Outline each uninfected red blood cell.
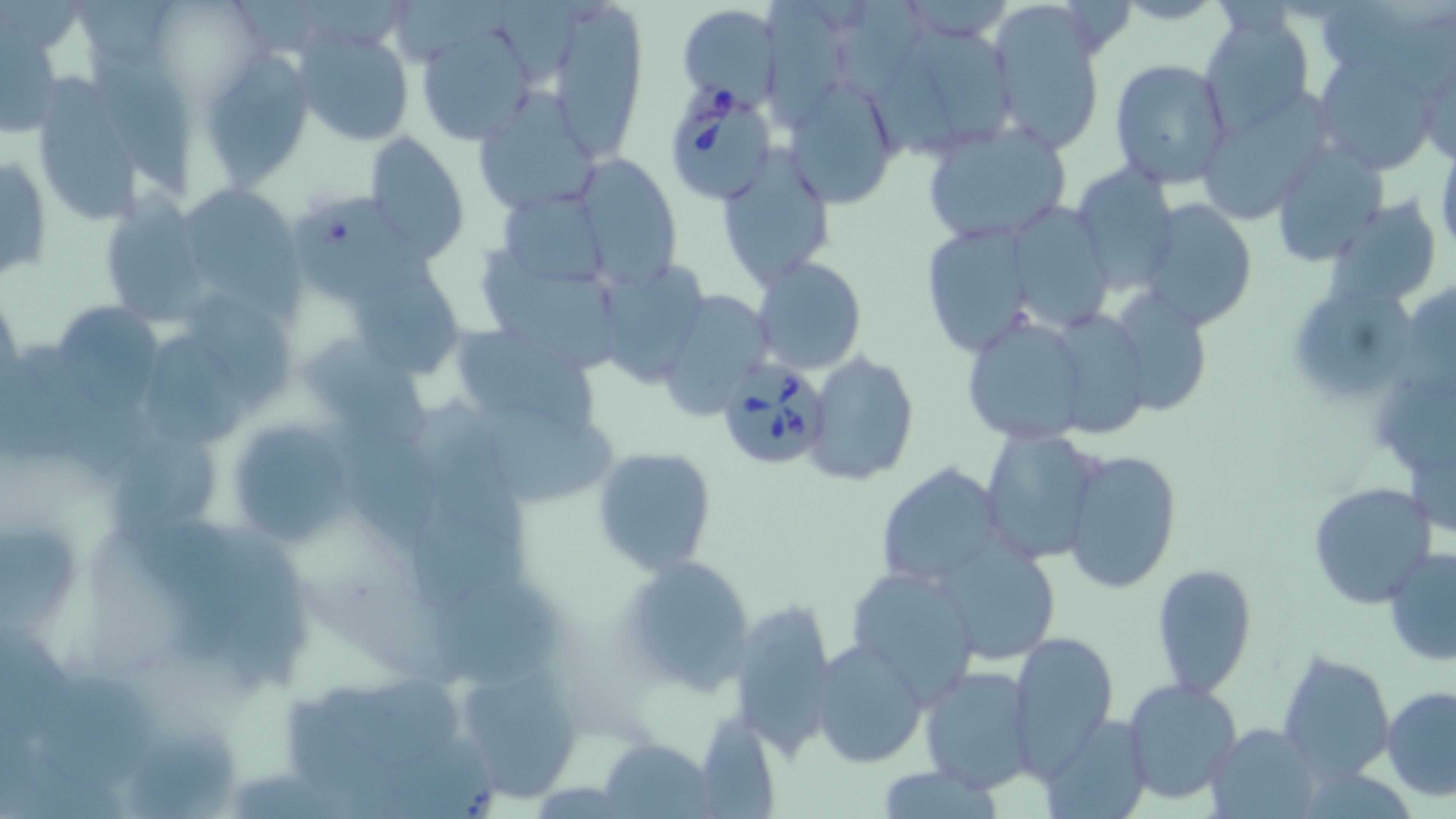
Approximate bounding boxes as named x1/y1/x2/y2 corners in pixels.
Uninfected red blood cells: (x1=548, y1=0, x2=648, y2=152), (x1=759, y1=3, x2=858, y2=128), (x1=986, y1=4, x2=1105, y2=157), (x1=677, y1=5, x2=779, y2=108), (x1=1199, y1=8, x2=1318, y2=137), (x1=914, y1=20, x2=1026, y2=145), (x1=414, y1=23, x2=536, y2=146), (x1=2, y1=24, x2=64, y2=135), (x1=295, y1=29, x2=414, y2=149), (x1=86, y1=43, x2=200, y2=201), (x1=199, y1=51, x2=315, y2=186), (x1=1313, y1=51, x2=1439, y2=173), (x1=1416, y1=52, x2=1455, y2=166), (x1=1109, y1=58, x2=1233, y2=189), (x1=785, y1=78, x2=900, y2=207), (x1=30, y1=79, x2=151, y2=230), (x1=472, y1=88, x2=603, y2=216), (x1=920, y1=122, x2=1073, y2=244), (x1=363, y1=131, x2=470, y2=263), (x1=1435, y1=141, x2=1456, y2=267), (x1=1271, y1=142, x2=1389, y2=267), (x1=716, y1=150, x2=835, y2=288), (x1=1, y1=154, x2=52, y2=282), (x1=574, y1=155, x2=681, y2=282), (x1=1069, y1=166, x2=1180, y2=295), (x1=184, y1=180, x2=310, y2=326), (x1=500, y1=191, x2=607, y2=290), (x1=98, y1=196, x2=211, y2=326), (x1=1329, y1=196, x2=1442, y2=308), (x1=1136, y1=197, x2=1258, y2=332), (x1=292, y1=198, x2=414, y2=302), (x1=1007, y1=201, x2=1118, y2=331), (x1=918, y1=221, x2=1037, y2=358), (x1=483, y1=245, x2=620, y2=366), (x1=346, y1=253, x2=459, y2=377), (x1=753, y1=256, x2=867, y2=374), (x1=603, y1=261, x2=707, y2=388), (x1=1298, y1=284, x2=1415, y2=402), (x1=1105, y1=289, x2=1213, y2=417), (x1=657, y1=291, x2=772, y2=418), (x1=58, y1=298, x2=164, y2=412), (x1=961, y1=315, x2=1092, y2=445), (x1=451, y1=319, x2=602, y2=435), (x1=25, y1=333, x2=144, y2=476), (x1=147, y1=335, x2=252, y2=449), (x1=306, y1=348, x2=436, y2=450), (x1=806, y1=352, x2=919, y2=486), (x1=483, y1=405, x2=622, y2=509), (x1=225, y1=417, x2=356, y2=548), (x1=315, y1=424, x2=444, y2=552), (x1=979, y1=427, x2=1107, y2=565), (x1=119, y1=432, x2=228, y2=544), (x1=591, y1=446, x2=718, y2=577), (x1=1060, y1=448, x2=1183, y2=595), (x1=411, y1=463, x2=535, y2=606), (x1=875, y1=463, x2=1005, y2=589), (x1=1308, y1=481, x2=1436, y2=608), (x1=928, y1=536, x2=1063, y2=666), (x1=1384, y1=545, x2=1456, y2=666), (x1=619, y1=553, x2=757, y2=694), (x1=1151, y1=562, x2=1258, y2=699), (x1=846, y1=566, x2=982, y2=706), (x1=434, y1=581, x2=561, y2=690), (x1=729, y1=598, x2=841, y2=754), (x1=1009, y1=631, x2=1118, y2=772), (x1=813, y1=641, x2=927, y2=770), (x1=1280, y1=649, x2=1396, y2=783), (x1=457, y1=661, x2=589, y2=801), (x1=918, y1=664, x2=1037, y2=792), (x1=30, y1=672, x2=156, y2=790), (x1=1121, y1=678, x2=1245, y2=806), (x1=320, y1=680, x2=468, y2=767), (x1=1381, y1=686, x2=1456, y2=801), (x1=1042, y1=712, x2=1152, y2=819), (x1=1205, y1=724, x2=1322, y2=816), (x1=125, y1=725, x2=244, y2=819), (x1=600, y1=737, x2=715, y2=817).

slide-level diagnosis = Babesia divergens
preparation = thin blood film
magnification = 1000x
stain = May-Grünwald-Giemsa
Babesia divergens-infected red blood cell locations = approximate bounding boxes as named x1/y1/x2/y2 corners in pixels: (x1=657, y1=74, x2=775, y2=201), (x1=712, y1=354, x2=827, y2=469)
image size = 1456×819 pixels
modality = optical microscopy
field of view = one of a larger specimen